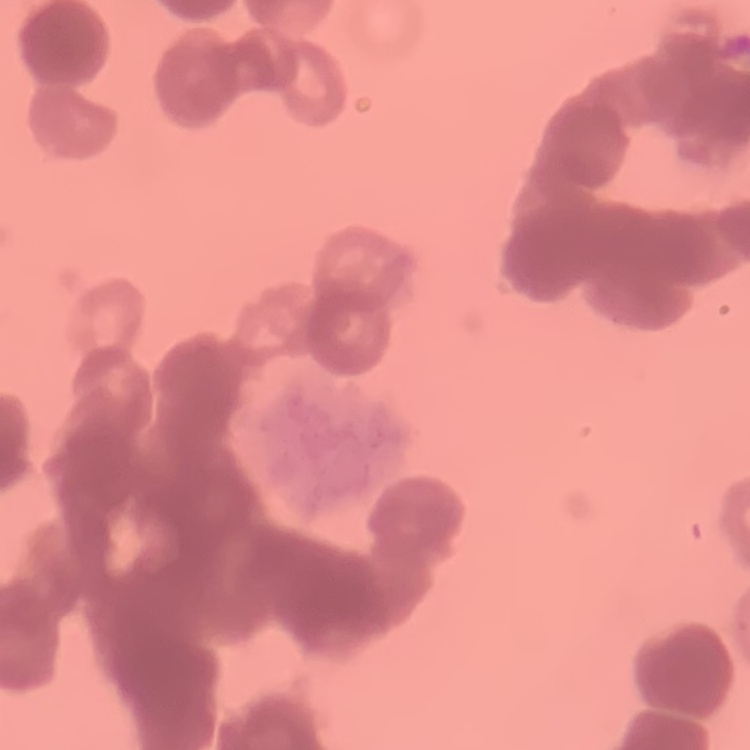
Summary:
  - Erythrocyte morphology: rouleaux formation
  - Stain: Field's or Giemsa
  - Preparation: thin peripheral smear
  - Image type: square crop of a larger photomicrograph